Name the blood parasite species.
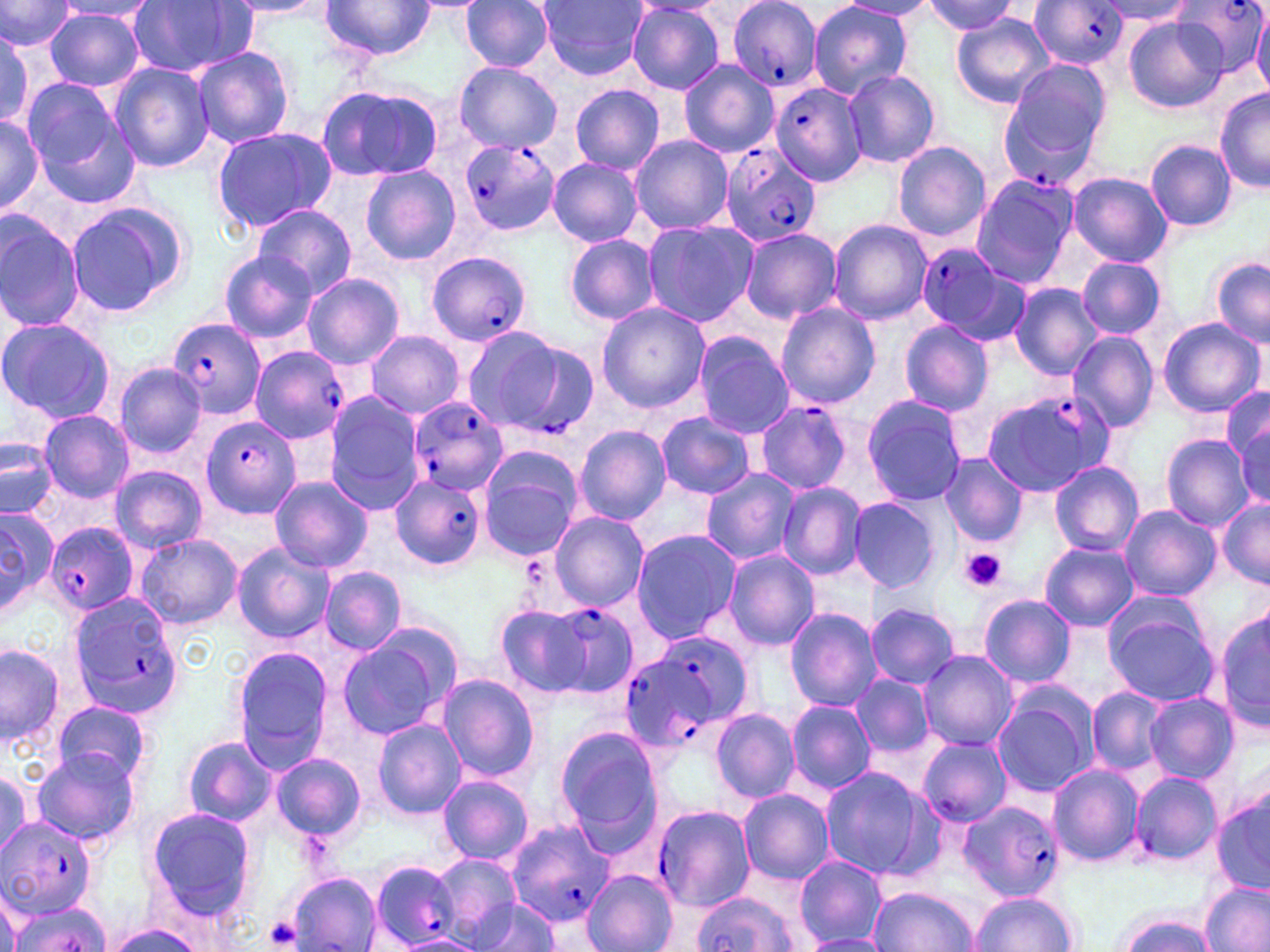
Plasmodium falciparum.

Summary:
  - Coordinate format: approximate bounding boxes as named x1/y1/x2/y2 corners in pixels
  - Platelet locations: (x1=958, y1=548, x2=1007, y2=592), (x1=263, y1=917, x2=303, y2=950)
  - Uninfected red blood cell locations (subset): (x1=539, y1=0, x2=649, y2=80), (x1=0, y1=1, x2=74, y2=54), (x1=125, y1=1, x2=256, y2=78), (x1=221, y1=1, x2=332, y2=20), (x1=321, y1=1, x2=438, y2=61), (x1=461, y1=1, x2=555, y2=72), (x1=808, y1=1, x2=914, y2=99), (x1=837, y1=1, x2=938, y2=19), (x1=1097, y1=1, x2=1197, y2=26), (x1=56, y1=2, x2=158, y2=22), (x1=918, y1=2, x2=1023, y2=36), (x1=627, y1=3, x2=726, y2=94), (x1=44, y1=8, x2=146, y2=92), (x1=1252, y1=9, x2=1270, y2=94), (x1=1124, y1=14, x2=1224, y2=115), (x1=951, y1=16, x2=1053, y2=109), (x1=0, y1=29, x2=42, y2=129), (x1=191, y1=47, x2=295, y2=148), (x1=998, y1=58, x2=1114, y2=150), (x1=678, y1=60, x2=778, y2=157), (x1=454, y1=61, x2=562, y2=153), (x1=109, y1=62, x2=216, y2=173), (x1=843, y1=69, x2=941, y2=169), (x1=21, y1=78, x2=124, y2=181), (x1=570, y1=84, x2=665, y2=174), (x1=315, y1=85, x2=443, y2=183), (x1=1215, y1=86, x2=1269, y2=193), (x1=35, y1=109, x2=142, y2=209), (x1=0, y1=112, x2=44, y2=217), (x1=211, y1=126, x2=336, y2=233), (x1=629, y1=134, x2=733, y2=234), (x1=1145, y1=140, x2=1237, y2=231), (x1=892, y1=141, x2=991, y2=243), (x1=548, y1=158, x2=643, y2=246), (x1=361, y1=164, x2=459, y2=264), (x1=1068, y1=173, x2=1171, y2=265), (x1=972, y1=175, x2=1079, y2=287), (x1=64, y1=201, x2=188, y2=317), (x1=251, y1=204, x2=355, y2=297), (x1=0, y1=211, x2=87, y2=332), (x1=827, y1=219, x2=933, y2=325), (x1=642, y1=220, x2=759, y2=327), (x1=740, y1=227, x2=841, y2=324), (x1=563, y1=233, x2=662, y2=325), (x1=217, y1=248, x2=319, y2=342), (x1=1079, y1=255, x2=1166, y2=339), (x1=1210, y1=257, x2=1270, y2=349), (x1=302, y1=272, x2=404, y2=368), (x1=1007, y1=282, x2=1105, y2=380), (x1=596, y1=301, x2=709, y2=414), (x1=775, y1=301, x2=880, y2=409), (x1=0, y1=317, x2=115, y2=424), (x1=1158, y1=318, x2=1266, y2=419), (x1=898, y1=320, x2=993, y2=417), (x1=462, y1=324, x2=571, y2=430), (x1=365, y1=330, x2=465, y2=419), (x1=1067, y1=330, x2=1160, y2=433), (x1=692, y1=331, x2=794, y2=436), (x1=116, y1=363, x2=206, y2=457), (x1=1221, y1=386, x2=1270, y2=474), (x1=323, y1=396, x2=422, y2=514), (x1=862, y1=396, x2=966, y2=508), (x1=38, y1=411, x2=134, y2=503), (x1=656, y1=412, x2=757, y2=500), (x1=1235, y1=419, x2=1269, y2=506), (x1=575, y1=426, x2=671, y2=526), (x1=1159, y1=434, x2=1254, y2=531), (x1=1, y1=435, x2=58, y2=520), (x1=477, y1=446, x2=583, y2=560), (x1=938, y1=453, x2=1027, y2=547), (x1=1048, y1=462, x2=1143, y2=555), (x1=110, y1=467, x2=209, y2=553), (x1=700, y1=469, x2=800, y2=566), (x1=269, y1=475, x2=373, y2=574), (x1=777, y1=481, x2=866, y2=581), (x1=848, y1=495, x2=942, y2=594), (x1=1217, y1=499, x2=1270, y2=587), (x1=1118, y1=504, x2=1220, y2=601), (x1=0, y1=505, x2=57, y2=619), (x1=548, y1=511, x2=648, y2=611), (x1=630, y1=530, x2=739, y2=643), (x1=133, y1=533, x2=242, y2=628), (x1=1040, y1=542, x2=1138, y2=630), (x1=232, y1=543, x2=332, y2=643), (x1=722, y1=549, x2=820, y2=650), (x1=320, y1=567, x2=406, y2=655), (x1=976, y1=593, x2=1076, y2=688), (x1=1102, y1=599, x2=1219, y2=705), (x1=494, y1=603, x2=596, y2=699), (x1=866, y1=603, x2=959, y2=689), (x1=1216, y1=605, x2=1269, y2=736), (x1=784, y1=607, x2=883, y2=710), (x1=337, y1=632, x2=455, y2=741), (x1=1, y1=642, x2=66, y2=751), (x1=231, y1=645, x2=334, y2=772), (x1=916, y1=650, x2=1017, y2=751), (x1=851, y1=673, x2=935, y2=759), (x1=436, y1=674, x2=540, y2=782), (x1=1087, y1=688, x2=1167, y2=775), (x1=990, y1=690, x2=1097, y2=797), (x1=1144, y1=692, x2=1239, y2=784), (x1=786, y1=699, x2=876, y2=796), (x1=53, y1=701, x2=152, y2=786), (x1=711, y1=708, x2=799, y2=801), (x1=371, y1=719, x2=466, y2=819), (x1=553, y1=724, x2=664, y2=846), (x1=180, y1=735, x2=275, y2=827), (x1=917, y1=737, x2=1012, y2=826), (x1=31, y1=749, x2=139, y2=847), (x1=269, y1=753, x2=367, y2=842), (x1=0, y1=763, x2=43, y2=856), (x1=1047, y1=764, x2=1144, y2=867), (x1=818, y1=767, x2=934, y2=877), (x1=1129, y1=770, x2=1223, y2=869), (x1=436, y1=773, x2=534, y2=864), (x1=1211, y1=786, x2=1270, y2=897), (x1=738, y1=789, x2=834, y2=884), (x1=142, y1=805, x2=257, y2=923), (x1=431, y1=854, x2=521, y2=942), (x1=793, y1=855, x2=889, y2=947), (x1=583, y1=870, x2=677, y2=952), (x1=287, y1=873, x2=382, y2=952), (x1=1200, y1=881, x2=1269, y2=952), (x1=0, y1=882, x2=22, y2=952), (x1=870, y1=887, x2=981, y2=952), (x1=967, y1=892, x2=1080, y2=951), (x1=468, y1=897, x2=561, y2=951), (x1=3, y1=900, x2=109, y2=952), (x1=1108, y1=911, x2=1223, y2=952), (x1=100, y1=923, x2=207, y2=952), (x1=388, y1=934, x2=483, y2=951), (x1=801, y1=935, x2=892, y2=952)
  - Plasmodium falciparum-infected red blood cell locations (subset): (x1=725, y1=0, x2=821, y2=93), (x1=1027, y1=0, x2=1131, y2=69), (x1=1171, y1=0, x2=1267, y2=79), (x1=769, y1=82, x2=867, y2=187), (x1=1000, y1=95, x2=1101, y2=194), (x1=458, y1=139, x2=561, y2=237), (x1=719, y1=143, x2=820, y2=248), (x1=914, y1=242, x2=1025, y2=343), (x1=427, y1=250, x2=534, y2=348), (x1=166, y1=319, x2=266, y2=421), (x1=498, y1=339, x2=599, y2=438), (x1=250, y1=348, x2=347, y2=446), (x1=982, y1=388, x2=1112, y2=497), (x1=407, y1=396, x2=508, y2=496), (x1=753, y1=399, x2=854, y2=495), (x1=200, y1=414, x2=300, y2=519), (x1=389, y1=477, x2=483, y2=570), (x1=45, y1=522, x2=138, y2=617), (x1=66, y1=593, x2=185, y2=717), (x1=542, y1=606, x2=634, y2=695), (x1=627, y1=631, x2=753, y2=746), (x1=650, y1=802, x2=753, y2=910), (x1=0, y1=817, x2=100, y2=917), (x1=505, y1=819, x2=618, y2=930), (x1=368, y1=859, x2=462, y2=949)
  - Stain: May-Grünwald-Giemsa
  - Field of view: one of a larger specimen
  - Image size: 1270×952 pixels
  - Magnification: 1000x
  - Modality: light microscopy
  - Preparation: thin blood smear